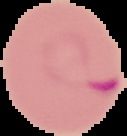
Image is 127×136 pixels. Malaria status: parasitized. Segmented cell region on a black background. From a thin blood smear.